Report the malaria status of this cell.
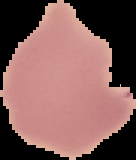

It is uninfected.

image size = 136×160 pixels
image type = cell region segmented out of the field of view; surrounding area masked to black
preparation = thin blood film